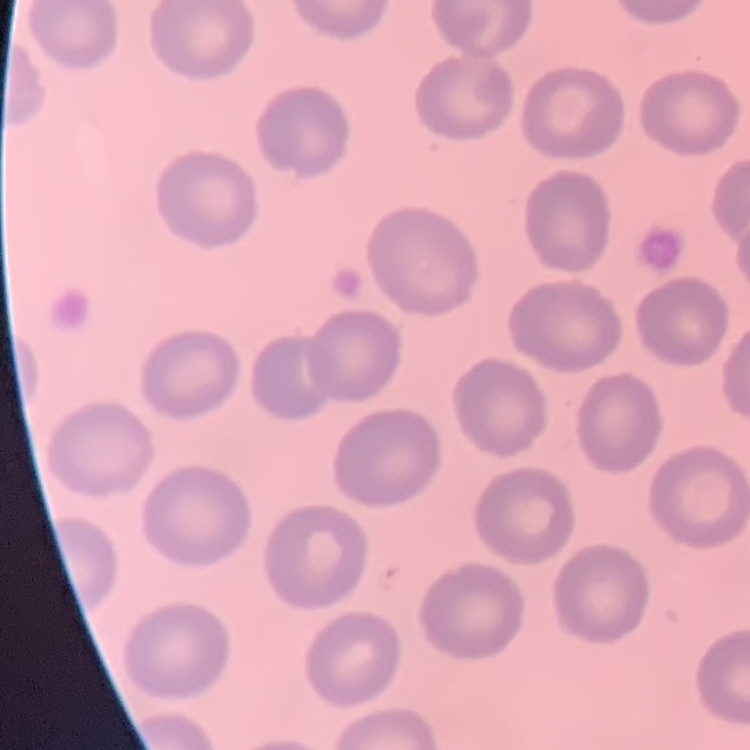
red blood cell morphology = no rouleaux formation
image type = square crop of a larger photomicrograph
stain = Field's or Giemsa
preparation = thin blood smear